Classify this cell by malaria status.
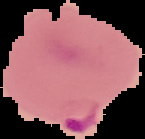
It is parasitized.

image size = 145×139 pixels
image type = segmented cell region on a black background
preparation = thin blood smear